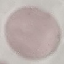

Result: no malaria parasites detected. Photographed with a smartphone camera at the microscope eyepiece. Giemsa stain. Automatically extracted cell patch, resized to 64 × 64 pixels. Thin smear of blood.